Give the position of every Plasmodium parasite.
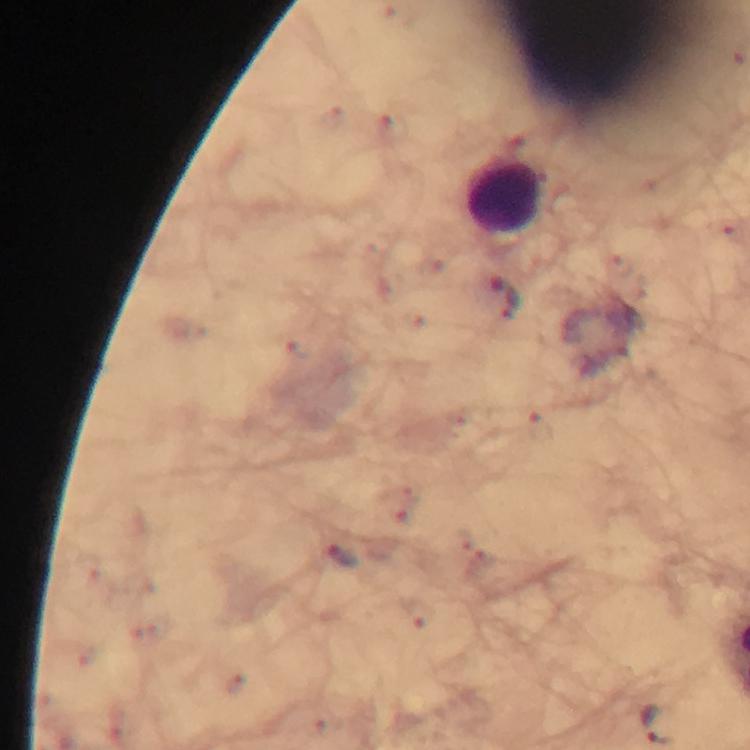
Approximate centers as {x, y} in pixels.
Plasmodium parasites: {505, 299}, {343, 556}.

Leukocyte locations: {504, 195}. Image is 750×750 pixels. Photographed through the microscope with a smartphone camera. Giemsa stain. A crop from one field of view. Immersion oil applied. 100x magnification. From a diagnostic examination for malaria. Thick blood film.